Describe the morphology of the erythrocytes.
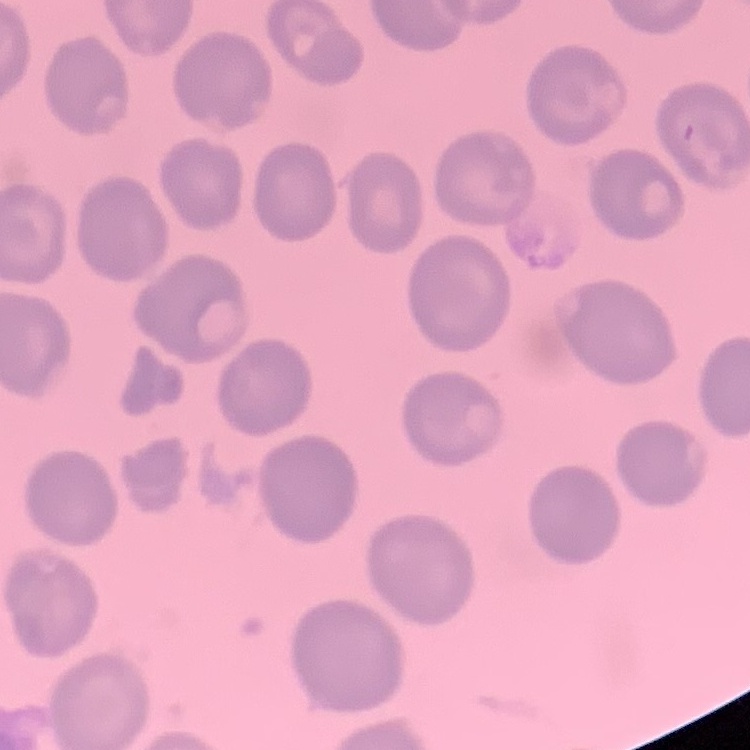

No rouleaux formation.

Square crop of a larger photomicrograph. Stained with either Field's or Giemsa. Thin blood smear.